Classify this cell by malaria status.
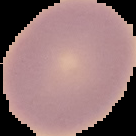
It is uninfected.

image type = segmented cell region on a black background
image size = 136×136 pixels
preparation = thin blood smear